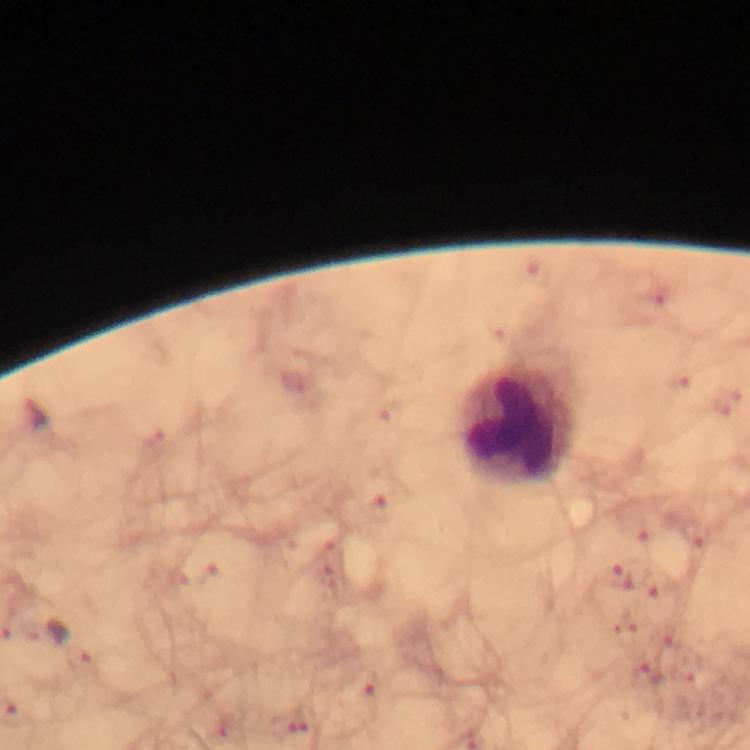
Approximate centers as {x, y} in pixels. Leukocyte locations: {519, 424}. Plasmodium parasite locations: {619, 575}, {652, 586}, {365, 685}. Smartphone photograph taken through a microscope. From a malaria diagnostic workup. 100x magnification. Image is 750×750 pixels. Thick smear. A crop from one field of view. Immersion oil applied. Giemsa-stained preparation.